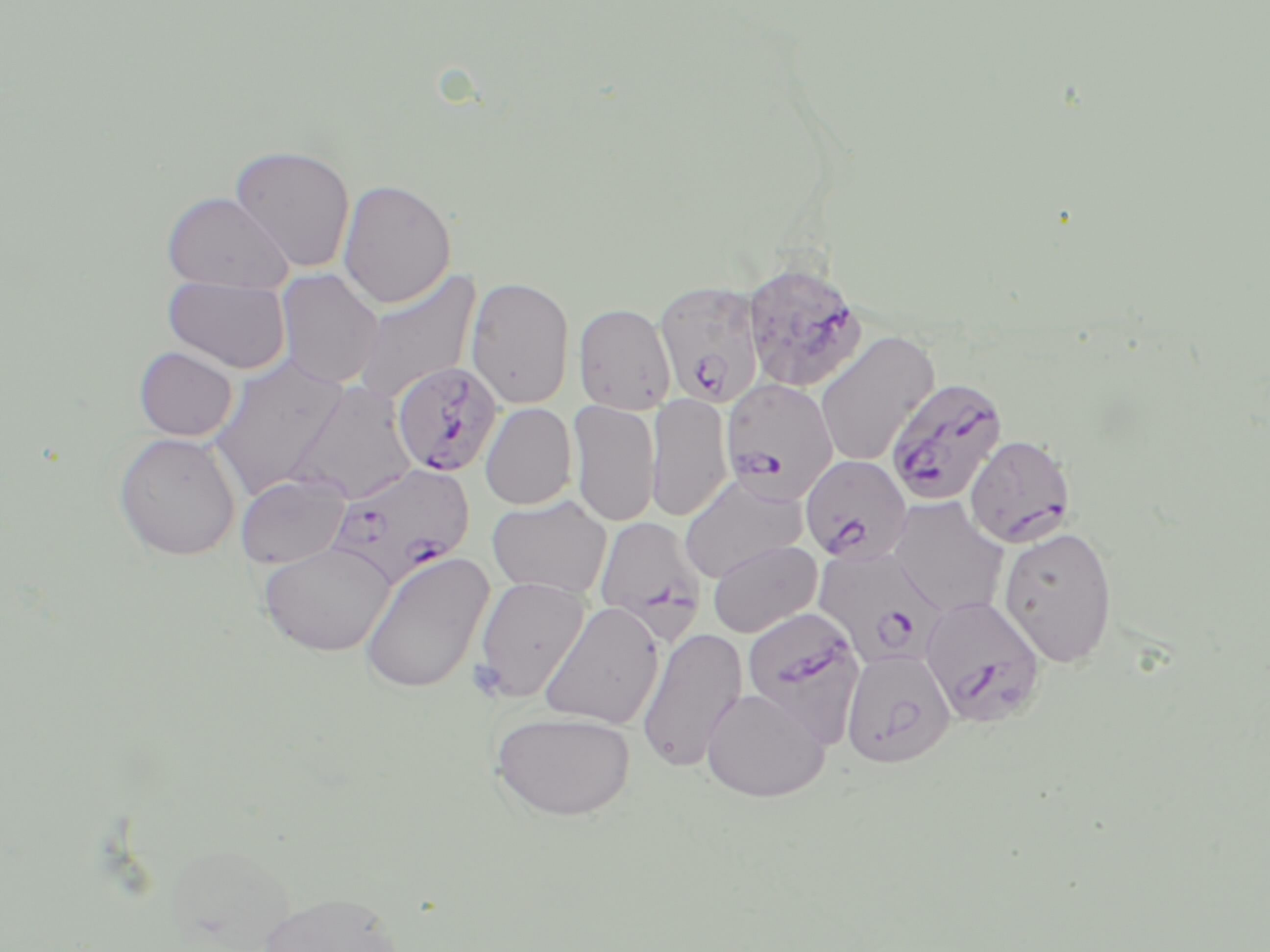
Approximate bounding boxes as named x1/y1/x2/y2 corners in pixels. Plasmodium falciparum-infected red blood cell locations: (x1=742, y1=259, x2=867, y2=393), (x1=654, y1=280, x2=765, y2=408), (x1=391, y1=361, x2=502, y2=476), (x1=885, y1=376, x2=1008, y2=505), (x1=721, y1=378, x2=839, y2=503), (x1=966, y1=434, x2=1077, y2=547), (x1=800, y1=454, x2=912, y2=564), (x1=327, y1=462, x2=475, y2=588), (x1=594, y1=516, x2=707, y2=644), (x1=814, y1=545, x2=948, y2=670), (x1=919, y1=595, x2=1047, y2=728), (x1=741, y1=606, x2=866, y2=744). Platelet locations: (x1=469, y1=659, x2=507, y2=700). Uninfected red blood cell locations: (x1=228, y1=144, x2=356, y2=273), (x1=338, y1=178, x2=457, y2=309), (x1=161, y1=191, x2=292, y2=293), (x1=352, y1=268, x2=483, y2=406), (x1=275, y1=269, x2=384, y2=388), (x1=163, y1=276, x2=292, y2=374), (x1=466, y1=276, x2=575, y2=409), (x1=574, y1=303, x2=676, y2=415), (x1=815, y1=331, x2=939, y2=467), (x1=134, y1=346, x2=238, y2=441), (x1=207, y1=355, x2=352, y2=499), (x1=287, y1=381, x2=417, y2=504), (x1=646, y1=393, x2=733, y2=522), (x1=567, y1=400, x2=660, y2=527), (x1=480, y1=402, x2=577, y2=509), (x1=112, y1=432, x2=242, y2=561), (x1=235, y1=472, x2=352, y2=569), (x1=679, y1=474, x2=807, y2=583), (x1=487, y1=496, x2=612, y2=598), (x1=887, y1=496, x2=1009, y2=618), (x1=998, y1=525, x2=1117, y2=668), (x1=708, y1=539, x2=821, y2=638), (x1=257, y1=542, x2=397, y2=657), (x1=359, y1=551, x2=494, y2=694), (x1=473, y1=575, x2=591, y2=702), (x1=538, y1=601, x2=664, y2=729), (x1=636, y1=626, x2=748, y2=774), (x1=841, y1=648, x2=956, y2=769), (x1=701, y1=687, x2=830, y2=802), (x1=490, y1=710, x2=637, y2=820), (x1=258, y1=889, x2=405, y2=952). Slide-level diagnosis: Plasmodium falciparum. One field of a larger specimen. Thin blood film. Optical microscopy. Image is 1270×952 pixels. 1000x magnification. May-Grünwald-Giemsa stain.